Classify this cell by malaria status.
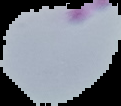
It is parasitized.

{
  "image_type": "segmented cell region with the area outside set to black",
  "preparation": "thin blood film",
  "image_size": "121×106 pixels"
}